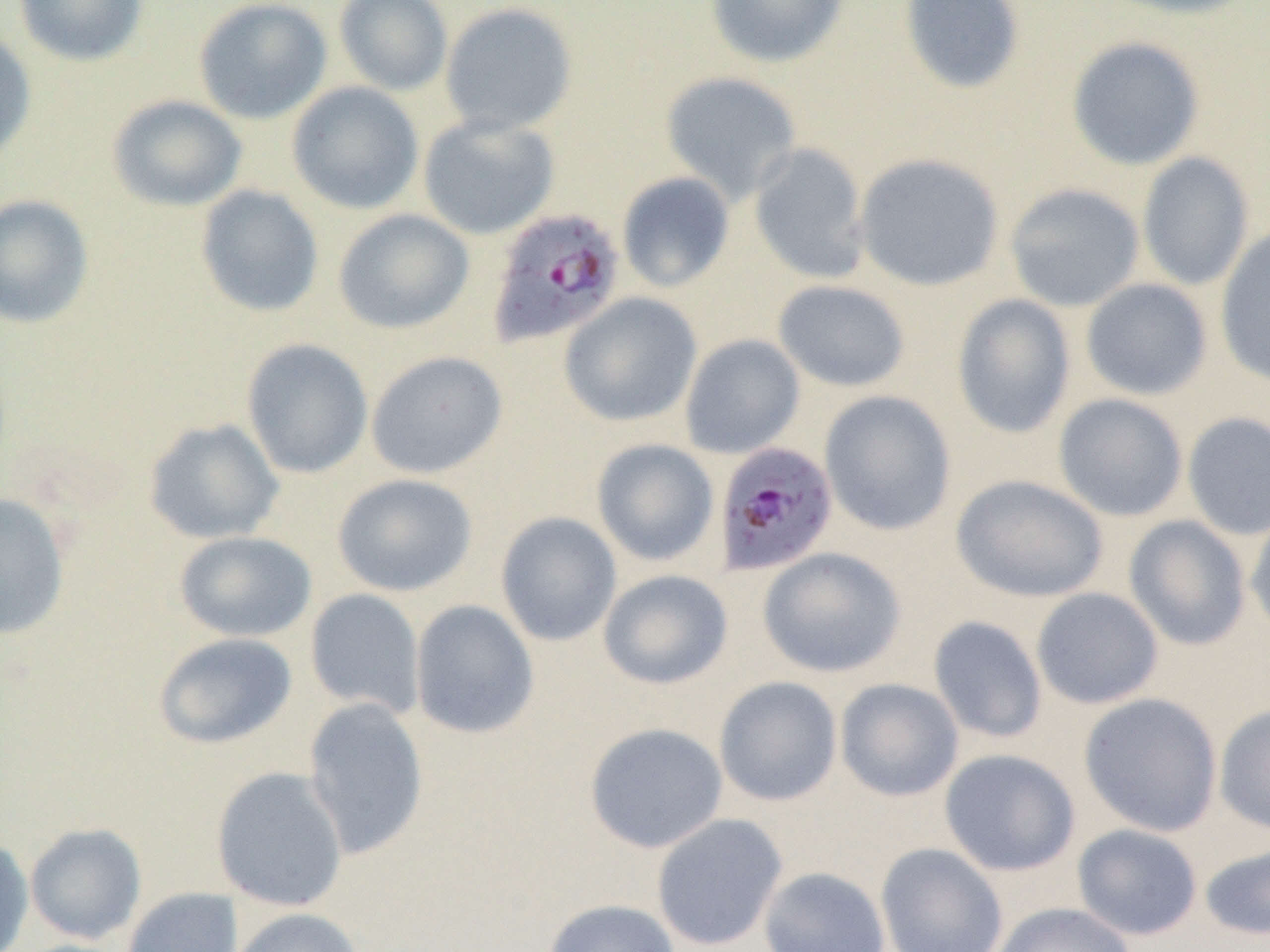
slide-level diagnosis = Plasmodium falciparum
image size = 1270×952 pixels
preparation = thin blood smear
field of view = one of a larger specimen
uninfected red blood cell locations = approximate bounding boxes as (x1,y1)-(x2,y2) corner pairs in pixels: (13,0)-(149,67), (193,0)-(333,125), (334,0)-(454,96), (705,0)-(849,69), (898,0)-(1026,94), (1102,0)-(1262,21), (439,2)-(579,136), (0,28)-(38,169), (1065,36)-(1206,170), (659,71)-(803,204), (286,81)-(424,215), (107,94)-(248,212), (417,114)-(561,240), (748,143)-(871,284), (854,152)-(1005,291), (1137,152)-(1255,292), (616,172)-(735,293), (1004,182)-(1145,312), (195,185)-(324,317), (0,194)-(95,329), (333,208)-(474,334), (1215,226)-(1270,388), (1080,278)-(1213,401), (772,279)-(912,392), (558,292)-(703,428), (951,293)-(1076,439), (679,334)-(805,459), (241,338)-(373,479), (365,350)-(508,479), (818,390)-(956,535), (1053,393)-(1188,522), (1182,412)-(1270,540), (144,418)-(284,544), (591,438)-(720,567), (332,473)-(477,597), (950,473)-(1109,603), (0,491)-(71,642), (1245,509)-(1270,638), (495,512)-(622,646), (1123,514)-(1252,651), (173,531)-(317,642), (757,547)-(906,678), (598,569)-(734,690), (1031,587)-(1163,710), (305,589)-(425,718), (409,599)-(539,739), (928,616)-(1048,744), (153,632)-(297,750), (713,676)-(843,807), (834,678)-(964,802), (1079,692)-(1222,837), (302,697)-(429,861), (1214,704)-(1270,835), (584,722)-(728,854), (939,748)-(1081,876), (210,766)-(349,912), (651,813)-(788,951), (25,823)-(147,944), (1072,823)-(1203,940), (0,835)-(34,952), (875,842)-(1008,952), (1199,842)-(1270,942), (758,866)-(891,952), (122,887)-(242,952), (542,899)-(680,952), (992,902)-(1135,952), (227,907)-(366,952)
magnification = 1000x
modality = optical microscopy
Plasmodium falciparum-infected red blood cell locations = approximate bounding boxes as (x1,y1)-(x2,y2) corner pairs in pixels: (485,207)-(626,349), (713,441)-(838,577)